Locate every Plasmodium parasite.
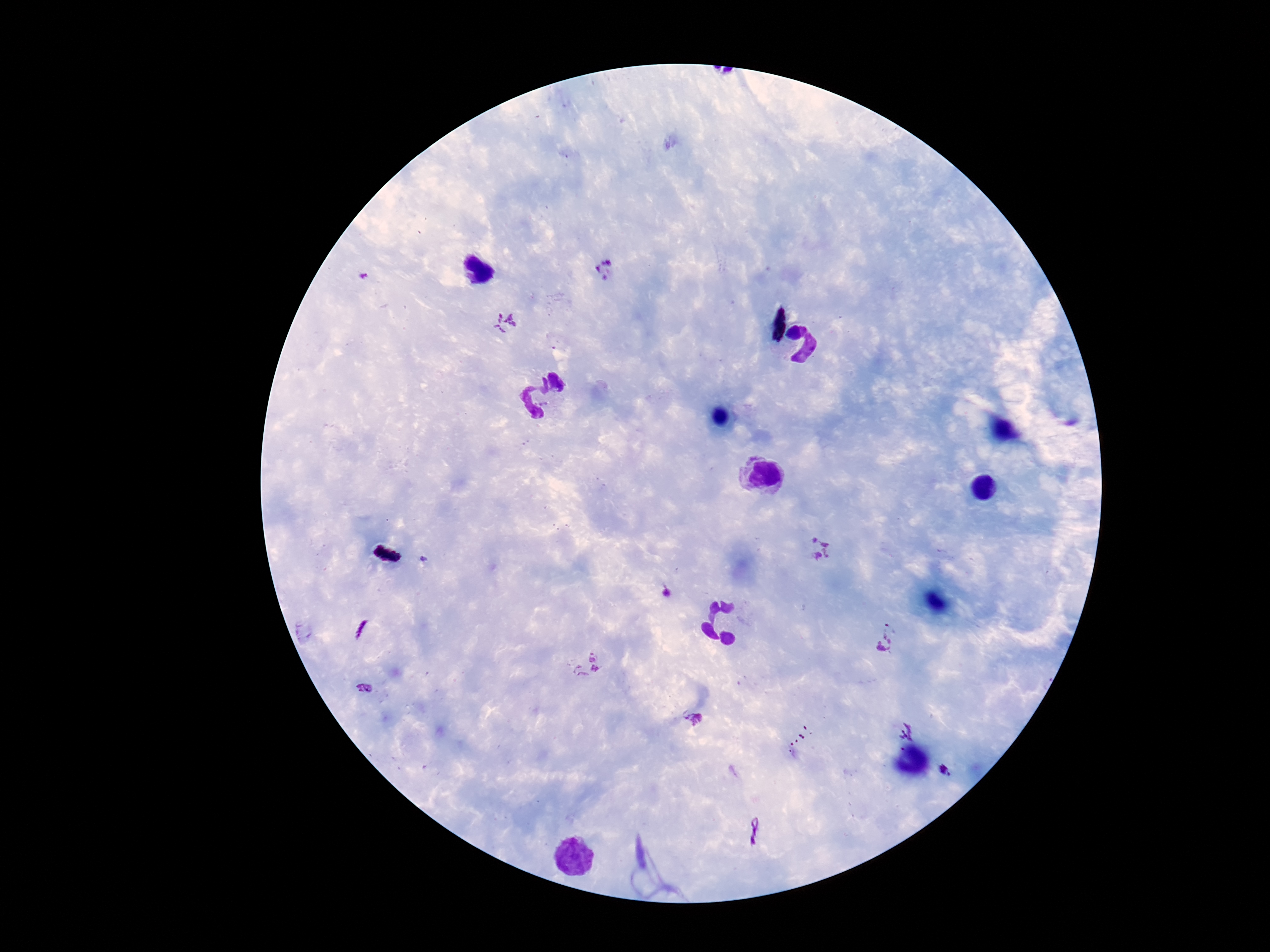
Approximate centers as (x, y) in pixels.
Plasmodium parasites: (607, 269), (363, 277), (504, 322), (816, 548), (887, 638), (587, 665), (365, 688), (694, 720), (907, 724), (945, 774), (753, 830).

{
  "stain": "Giemsa",
  "field_of_view": "single",
  "preparation": "thick blood film",
  "patient_malaria_status": "infected",
  "capture": "smartphone camera through the microscope eyepiece",
  "image_size": "1270×952 pixels",
  "magnification": "100x"
}